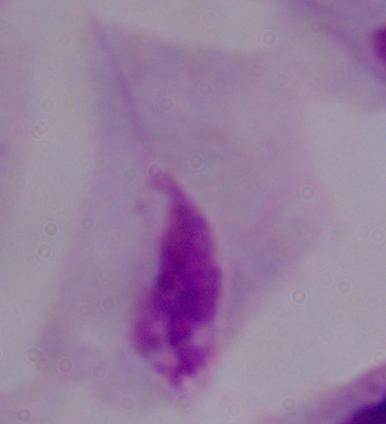

A trichomonad is seen. 1000x magnification. Micrograph.